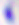
modality = photomicrograph
magnification = 400x
identification = Toxoplasma gondii